Assess this cell for malaria.
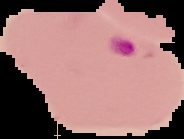
It is parasitized.

Summary:
  - Preparation: thin blood smear
  - Image size: 184×139 pixels
  - Image type: segmented cell region on a black background